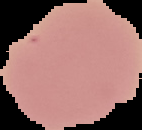 From a thin blood smear. Segmented cell region on a black background. Result: negative for Plasmodium parasites. Image is 142×130 pixels.